Classify this cell by malaria status.
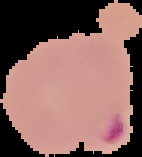
It is parasitized.

preparation = thin blood film
image type = segmented cell region with the area outside set to black
image size = 142×157 pixels